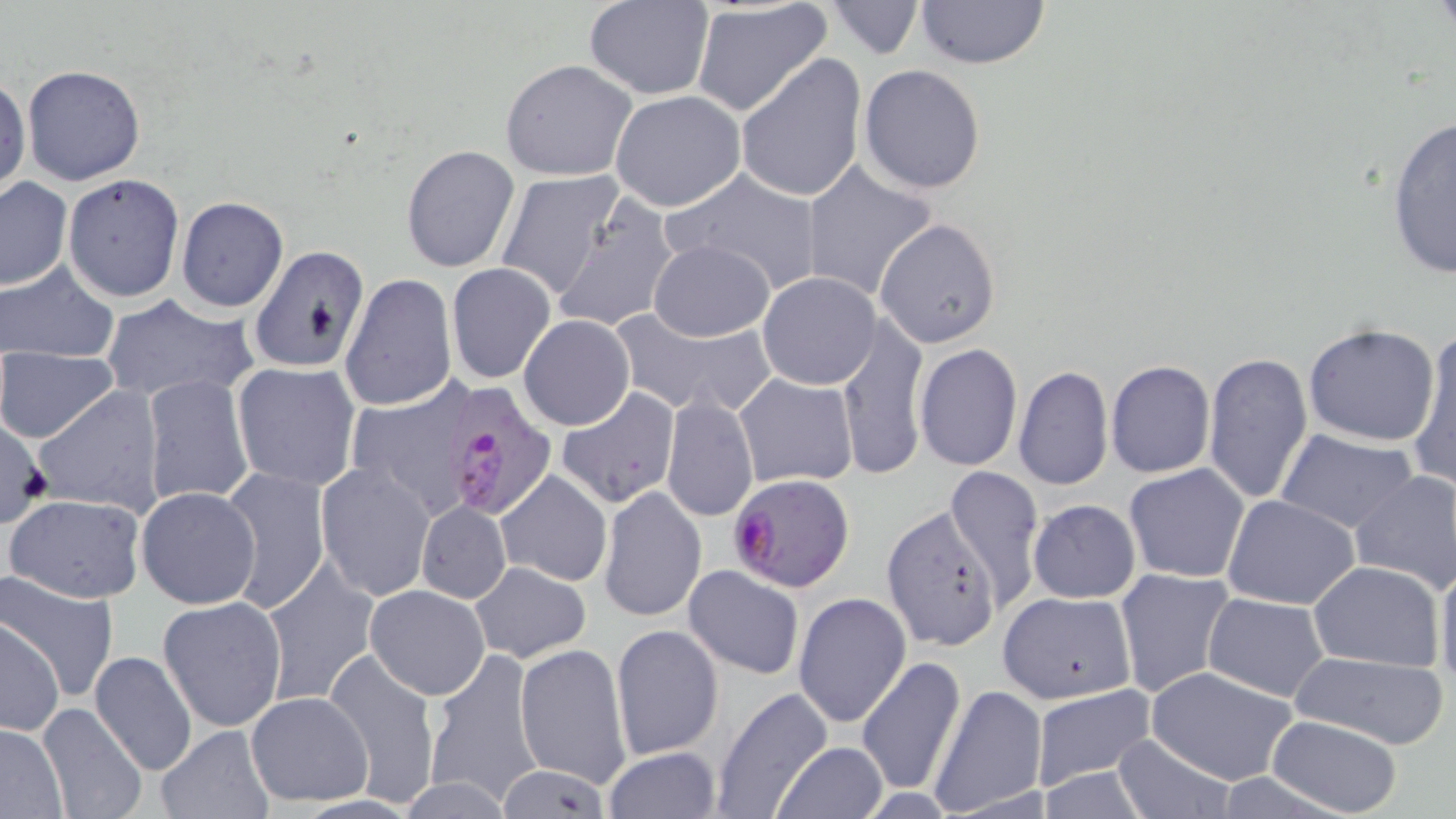
Approximate bounding boxes as (x1, y1, x2, y2) in pixels. Uninfected red blood cell locations: (584, 0, 712, 98), (913, 0, 1052, 69), (825, 2, 924, 59), (691, 3, 833, 118), (736, 53, 867, 205), (500, 59, 638, 180), (20, 64, 147, 186), (859, 64, 986, 195), (652, 66, 822, 194), (0, 73, 29, 193), (609, 90, 746, 211), (1387, 114, 1456, 282), (401, 145, 521, 272), (797, 160, 939, 300), (664, 167, 824, 294), (496, 170, 626, 302), (63, 173, 184, 303), (0, 177, 73, 292), (549, 194, 680, 334), (174, 196, 289, 312), (874, 218, 1001, 349), (648, 239, 774, 341), (250, 246, 371, 375), (1, 261, 119, 363), (446, 262, 556, 384), (758, 273, 880, 390), (340, 274, 455, 412), (100, 294, 261, 405), (609, 308, 774, 417), (519, 315, 635, 431), (836, 316, 930, 481), (1302, 324, 1443, 447), (1410, 329, 1456, 494), (915, 344, 1023, 471), (0, 347, 118, 444), (1202, 352, 1313, 507), (1105, 359, 1216, 479), (231, 362, 361, 491), (1013, 365, 1111, 491), (734, 373, 857, 489), (143, 375, 253, 507), (349, 377, 469, 517), (34, 385, 166, 516), (557, 386, 681, 509), (661, 394, 758, 523), (1276, 429, 1419, 533), (315, 463, 435, 601), (1124, 464, 1250, 583), (944, 465, 1045, 611), (219, 467, 331, 614), (494, 468, 613, 588), (1348, 470, 1456, 594), (598, 485, 706, 623), (135, 486, 262, 609), (4, 493, 146, 602), (1222, 494, 1361, 610), (1027, 499, 1141, 603), (416, 502, 511, 603), (881, 506, 1002, 654), (1436, 554, 1456, 695), (261, 557, 379, 707), (1307, 559, 1444, 669), (471, 561, 592, 663), (682, 565, 804, 679), (1114, 568, 1233, 697), (1, 572, 119, 703), (365, 585, 489, 700), (792, 592, 910, 728), (997, 592, 1137, 705), (1203, 594, 1328, 702), (157, 596, 286, 732), (1, 620, 65, 736), (611, 622, 723, 759), (514, 642, 634, 787), (422, 648, 545, 808), (321, 649, 440, 808), (88, 650, 198, 776), (1289, 650, 1450, 748), (857, 656, 966, 797), (1145, 667, 1300, 785), (926, 683, 1050, 818), (711, 684, 834, 817), (1029, 684, 1156, 791), (246, 691, 372, 805), (35, 704, 149, 819), (1265, 715, 1405, 817), (0, 723, 68, 818), (152, 724, 273, 818), (1111, 733, 1235, 819), (774, 741, 887, 818), (602, 746, 723, 819), (495, 763, 608, 817). Plasmodium falciparum-infected red blood cell locations: (443, 385, 555, 518), (728, 474, 855, 593). Slide-level diagnosis: Plasmodium falciparum. May-Grünwald-Giemsa stain. Image is 1456×819 pixels. Thin blood film. Light microscopy. Captured at 1000x magnification. One field of a larger specimen.